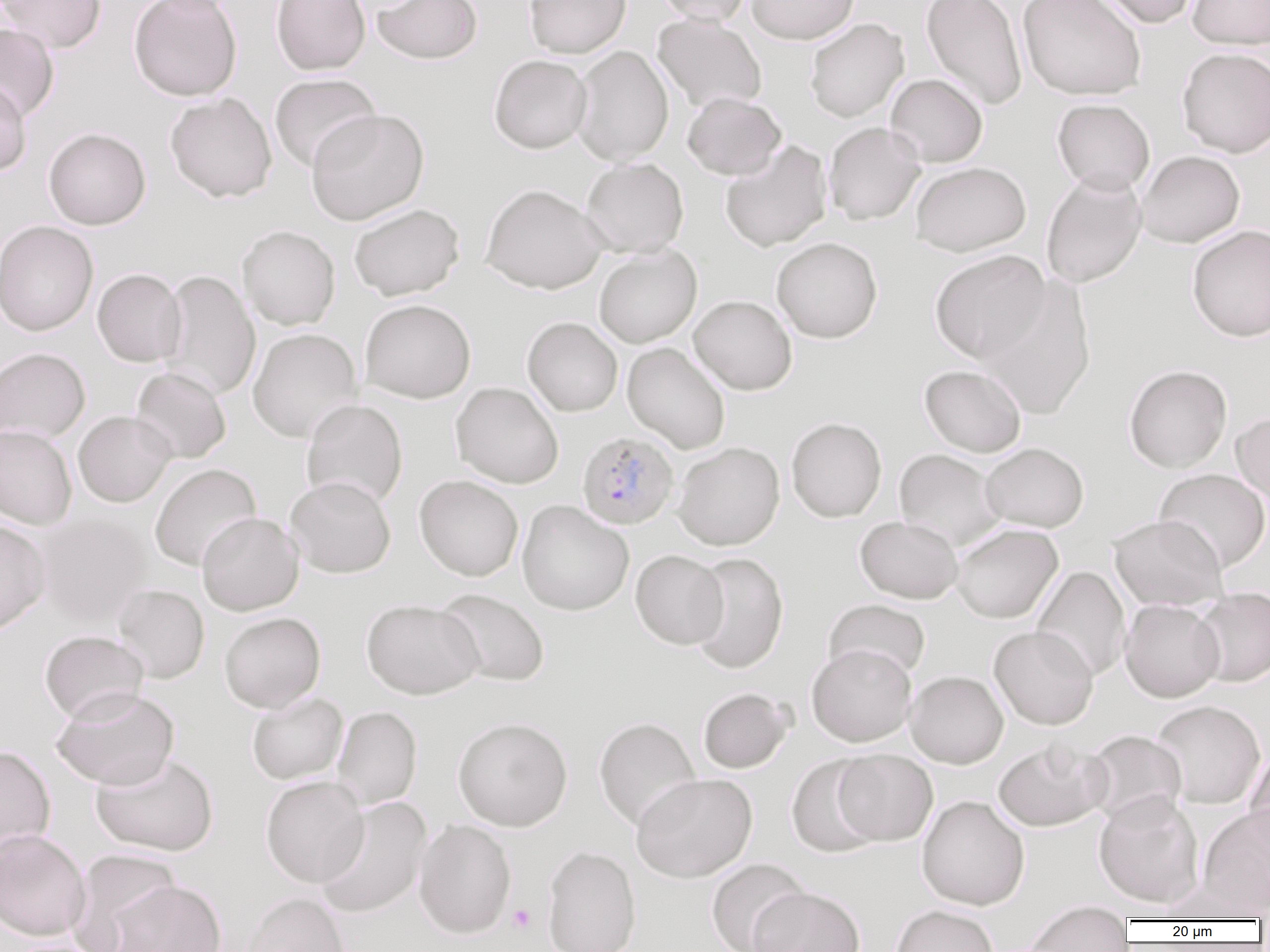

Approximate bounding boxes as (x1,y1)-(x2,y2) corner pairs in pixels. Platelet locations: (508,903)-(536,934). Uninfected red blood cell locations: (0,0)-(107,53), (129,0)-(243,101), (271,0)-(371,75), (371,0)-(482,64), (524,0)-(631,58), (655,0)-(753,25), (747,0)-(860,44), (920,0)-(1028,111), (1017,0)-(1147,101), (1094,0)-(1199,28), (1187,0)-(1270,49), (652,13)-(767,114), (804,18)-(909,122), (0,23)-(59,122), (571,45)-(674,165), (1177,47)-(1270,158), (489,54)-(592,154), (269,73)-(381,173), (886,73)-(988,167), (0,79)-(32,175), (165,92)-(277,203), (682,92)-(786,180), (1052,98)-(1155,194), (306,108)-(429,225), (824,122)-(926,225), (43,127)-(151,230), (720,140)-(833,252), (1136,150)-(1245,248), (581,157)-(689,257), (910,161)-(1031,256), (1041,171)-(1147,288), (480,183)-(609,294), (349,203)-(465,300), (0,220)-(99,337), (1187,224)-(1270,342), (237,225)-(340,330), (771,236)-(883,343), (594,245)-(702,347), (929,249)-(1051,363), (92,268)-(186,367), (159,270)-(260,401), (978,277)-(1097,420), (689,295)-(797,395), (359,298)-(476,404), (522,316)-(623,416), (247,328)-(363,442), (622,342)-(730,454), (0,348)-(90,444), (1124,364)-(1232,473), (919,365)-(1027,457), (131,367)-(231,464), (450,382)-(564,489), (301,399)-(408,509), (73,411)-(176,507), (1231,411)-(1270,507), (786,417)-(887,522), (0,425)-(77,530), (673,442)-(785,550), (980,442)-(1089,532), (893,449)-(1007,551), (150,463)-(261,571), (1154,468)-(1270,572), (414,474)-(523,581), (285,475)-(396,578), (516,500)-(634,615), (197,512)-(304,616), (36,514)-(151,626), (1108,515)-(1228,610), (854,516)-(963,603), (0,518)-(51,635), (951,523)-(1063,623), (630,549)-(728,649), (687,552)-(788,674), (1032,566)-(1131,681), (112,584)-(210,684), (1192,587)-(1270,687), (434,588)-(550,687), (1120,598)-(1225,702), (361,599)-(483,699), (823,599)-(931,682), (219,612)-(325,712), (988,625)-(1098,730), (39,630)-(149,723), (806,643)-(917,747), (905,670)-(1008,768), (51,687)-(179,790), (697,687)-(793,773), (246,691)-(348,785), (1150,700)-(1266,810), (332,706)-(422,810), (452,716)-(573,831), (593,717)-(701,830), (1082,729)-(1187,826), (992,739)-(1110,832), (0,745)-(56,861), (1244,748)-(1270,856), (832,749)-(938,846), (90,751)-(218,856), (787,754)-(885,858), (631,772)-(757,882), (260,775)-(369,888), (1093,791)-(1205,909), (917,795)-(1030,910), (314,796)-(432,919), (1197,805)-(1270,915), (414,819)-(517,938), (0,829)-(91,941), (541,845)-(642,952), (67,849)-(181,951), (705,858)-(810,952), (1157,879)-(1265,922), (106,880)-(226,951), (749,886)-(865,952), (241,892)-(352,952), (1023,903)-(1134,951), (890,904)-(999,952), (6,938)-(112,952). Plasmodium falciparum-infected red blood cell locations: (577,430)-(680,530). Slide-level diagnosis: Plasmodium falciparum. Image is 1270×952 pixels. Thin blood film. Single field of view. Light microscopy. Captured at 1000x magnification.